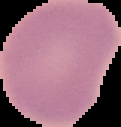

Summary:
  - Image size: 121×127 pixels
  - Result: no Plasmodium parasites detected
  - Preparation: thin blood film
  - Image type: segmented cell region with the area outside set to black